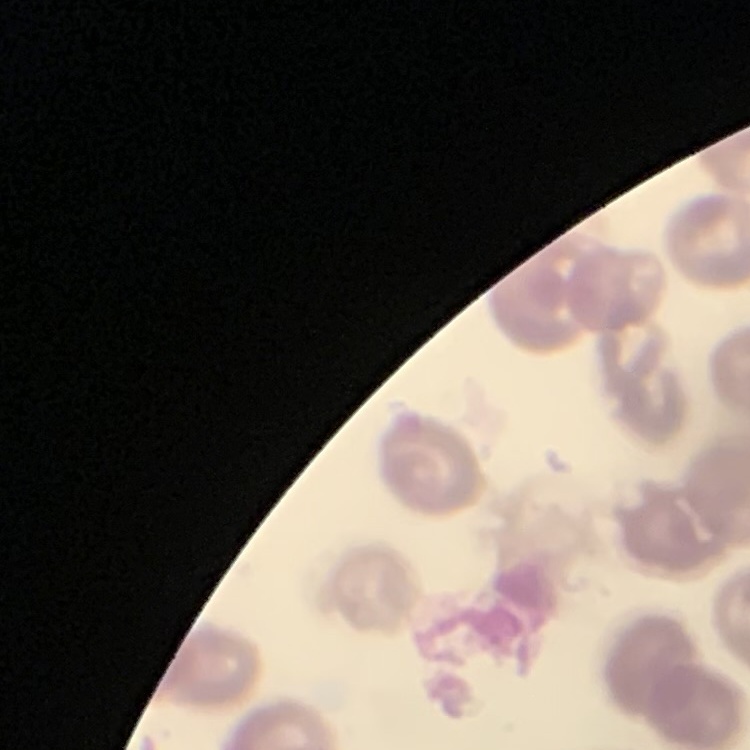
The erythrocytes show no rouleaux formation. Thin blood smear. Field's or Giemsa stain. One tile cut from a larger photomicrograph.